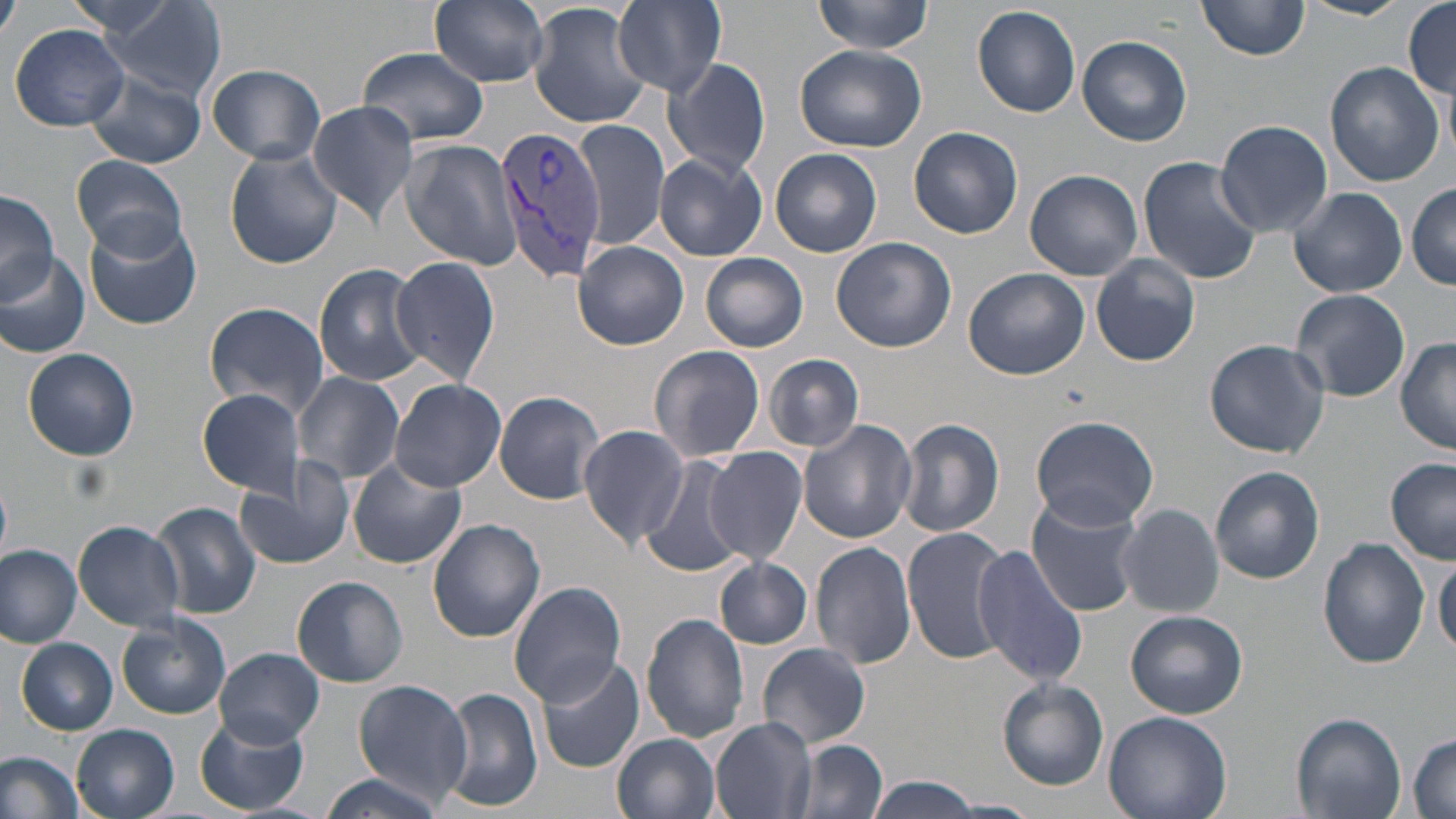
{
  "slide_level_diagnosis": "Plasmodium vivax",
  "field_of_view": "single",
  "image_size": "1456×819 pixels",
  "modality": "optical microscopy",
  "stain": "May-Grünwald-Giemsa",
  "preparation": "thin blood film",
  "uninfected_red_blood_cell_locations": "approximate bounding boxes as named x1/y1/x2/y2 corners in pixels: (x1=95, y1=0, x2=225, y2=101), (x1=431, y1=0, x2=549, y2=88), (x1=613, y1=0, x2=728, y2=95), (x1=812, y1=0, x2=937, y2=54), (x1=1198, y1=0, x2=1310, y2=60), (x1=1302, y1=0, x2=1410, y2=20), (x1=0, y1=2, x2=20, y2=44), (x1=1403, y1=2, x2=1456, y2=97), (x1=527, y1=3, x2=655, y2=130), (x1=972, y1=3, x2=1080, y2=119), (x1=8, y1=23, x2=131, y2=132), (x1=1077, y1=35, x2=1192, y2=146), (x1=795, y1=43, x2=929, y2=152), (x1=359, y1=46, x2=489, y2=147), (x1=664, y1=58, x2=771, y2=178), (x1=1324, y1=61, x2=1446, y2=186), (x1=204, y1=64, x2=327, y2=165), (x1=86, y1=73, x2=206, y2=166), (x1=307, y1=100, x2=417, y2=225), (x1=573, y1=119, x2=670, y2=251), (x1=1214, y1=119, x2=1333, y2=239), (x1=910, y1=127, x2=1024, y2=240), (x1=403, y1=138, x2=520, y2=274), (x1=225, y1=148, x2=341, y2=268), (x1=771, y1=148, x2=882, y2=257), (x1=655, y1=152, x2=767, y2=261), (x1=73, y1=155, x2=188, y2=257), (x1=1138, y1=156, x2=1261, y2=284), (x1=1025, y1=169, x2=1144, y2=281), (x1=1407, y1=183, x2=1456, y2=290), (x1=1289, y1=185, x2=1407, y2=297), (x1=0, y1=191, x2=58, y2=304), (x1=84, y1=216, x2=204, y2=330), (x1=831, y1=236, x2=957, y2=354), (x1=573, y1=242, x2=689, y2=350), (x1=699, y1=252, x2=808, y2=352), (x1=0, y1=254, x2=92, y2=360), (x1=1090, y1=254, x2=1200, y2=368), (x1=391, y1=255, x2=502, y2=388), (x1=314, y1=263, x2=430, y2=387), (x1=963, y1=267, x2=1089, y2=381), (x1=1288, y1=288, x2=1411, y2=403), (x1=203, y1=301, x2=333, y2=418), (x1=1204, y1=338, x2=1331, y2=458), (x1=1395, y1=338, x2=1456, y2=454), (x1=649, y1=345, x2=765, y2=462), (x1=21, y1=348, x2=139, y2=461), (x1=764, y1=353, x2=865, y2=451), (x1=294, y1=372, x2=405, y2=484), (x1=390, y1=378, x2=507, y2=491), (x1=198, y1=389, x2=307, y2=496), (x1=493, y1=390, x2=606, y2=504), (x1=1030, y1=415, x2=1159, y2=531), (x1=897, y1=419, x2=1005, y2=538), (x1=798, y1=420, x2=916, y2=545), (x1=579, y1=426, x2=689, y2=544), (x1=704, y1=446, x2=808, y2=565), (x1=235, y1=457, x2=356, y2=571), (x1=347, y1=457, x2=468, y2=570), (x1=639, y1=457, x2=753, y2=579), (x1=1386, y1=458, x2=1455, y2=564), (x1=1209, y1=465, x2=1325, y2=584), (x1=1027, y1=495, x2=1143, y2=617), (x1=152, y1=501, x2=261, y2=618), (x1=1116, y1=503, x2=1225, y2=618), (x1=73, y1=519, x2=187, y2=632), (x1=427, y1=519, x2=545, y2=643), (x1=904, y1=528, x2=1013, y2=666), (x1=1318, y1=537, x2=1430, y2=668), (x1=810, y1=540, x2=917, y2=670), (x1=0, y1=544, x2=82, y2=648), (x1=971, y1=545, x2=1088, y2=686), (x1=715, y1=557, x2=813, y2=649), (x1=1432, y1=557, x2=1456, y2=658), (x1=292, y1=576, x2=407, y2=687), (x1=509, y1=582, x2=626, y2=703), (x1=1125, y1=610, x2=1248, y2=719), (x1=642, y1=612, x2=751, y2=744), (x1=116, y1=613, x2=232, y2=719), (x1=17, y1=638, x2=117, y2=735), (x1=756, y1=644, x2=871, y2=749), (x1=214, y1=648, x2=326, y2=747), (x1=537, y1=655, x2=645, y2=774), (x1=997, y1=678, x2=1109, y2=790), (x1=354, y1=681, x2=472, y2=804), (x1=441, y1=687, x2=542, y2=813), (x1=1103, y1=710, x2=1232, y2=819), (x1=193, y1=713, x2=309, y2=815), (x1=1290, y1=713, x2=1406, y2=819), (x1=710, y1=717, x2=816, y2=819), (x1=72, y1=724, x2=180, y2=819), (x1=613, y1=732, x2=719, y2=819), (x1=1408, y1=733, x2=1456, y2=818), (x1=792, y1=738, x2=887, y2=819), (x1=0, y1=750, x2=85, y2=819), (x1=317, y1=771, x2=446, y2=819), (x1=865, y1=776, x2=988, y2=818)",
  "plasmodium_vivax_infected_red_blood_cell_locations": "approximate bounding boxes as named x1/y1/x2/y2 corners in pixels: (x1=496, y1=124, x2=608, y2=283)",
  "magnification": "1000x"
}